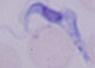

Summary:
  - Modality: micrograph
  - Magnification: 1000x
  - Identification: trypanosome